Classify this cell by malaria status.
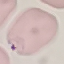
Parasitized.

Thin blood film. Acquired by smartphone through the microscope eyepiece. Automatically extracted cell patch, resized to 64 × 64 pixels. Giemsa-stained preparation.